Assess this cell for malaria.
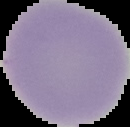
Uninfected.

{
  "image_size": "130×127 pixels",
  "image_type": "segmented cell region on a black background",
  "preparation": "thin blood smear"
}